Assess this cell for malaria.
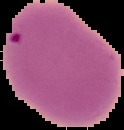
It is uninfected.

Summary:
  - Preparation: thin blood smear
  - Image size: 124×130 pixels
  - Image type: cell region segmented out of the field of view; surrounding area masked to black